Name the cell type shown.
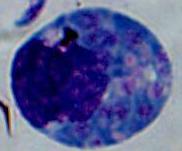
This is a leukocyte.

magnification = 1000x
modality = micrograph